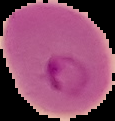
image size = 115×121 pixels
preparation = thin blood film
image type = cell region segmented out of the field of view; surrounding area masked to black
result = malaria parasites detected